Identify the preparation type.
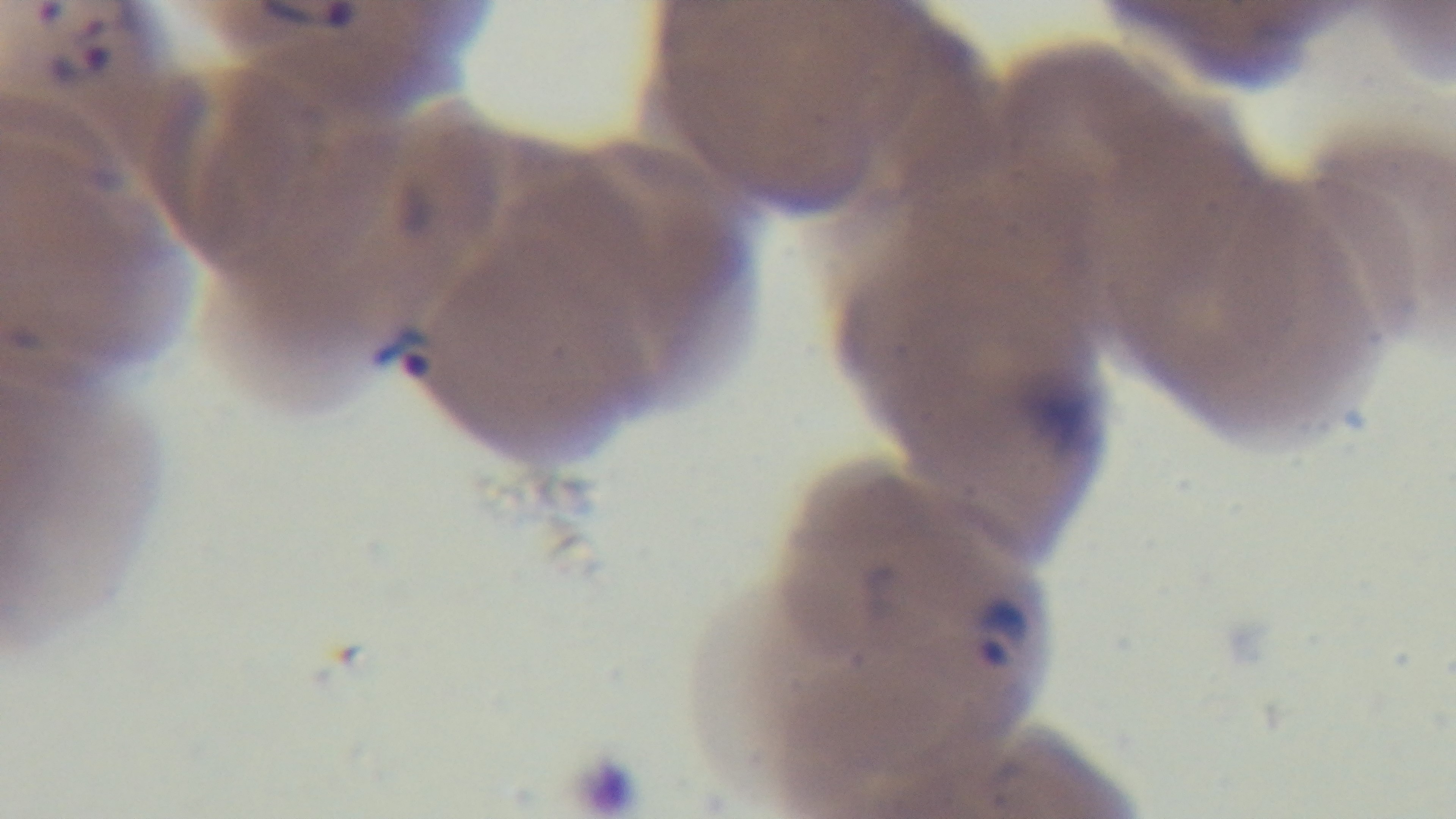

Thin.

Summary:
  - Modality: light microscopy
  - Objective: 100x oil immersion
  - Malaria status: positive
  - Field of view: single
  - Capture: mounted 4K digital camera
  - Stain: Giemsa